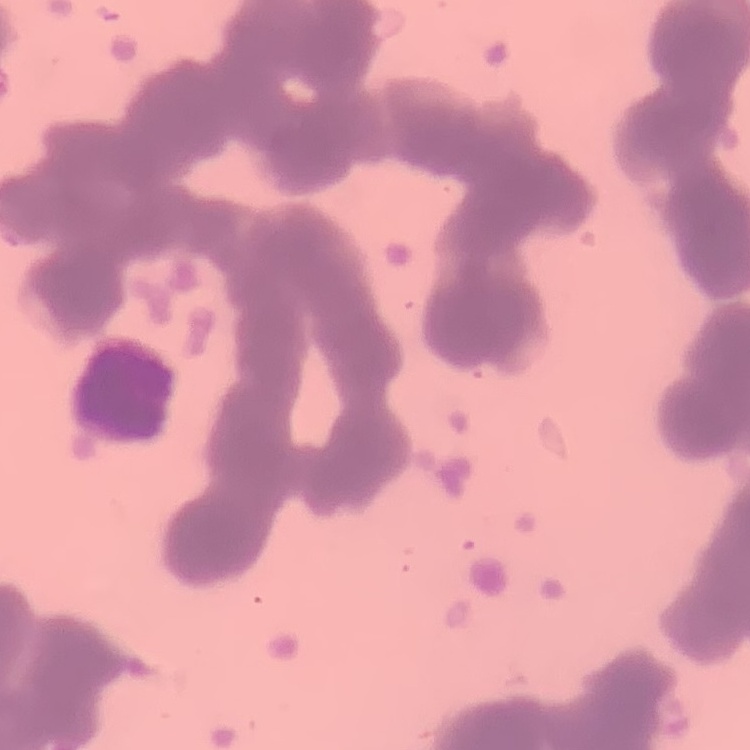
Summary:
  - Erythrocyte morphology: rouleaux formation
  - Stain: Field's or Giemsa
  - Preparation: thin blood smear
  - Image type: one tile cut from a larger photomicrograph